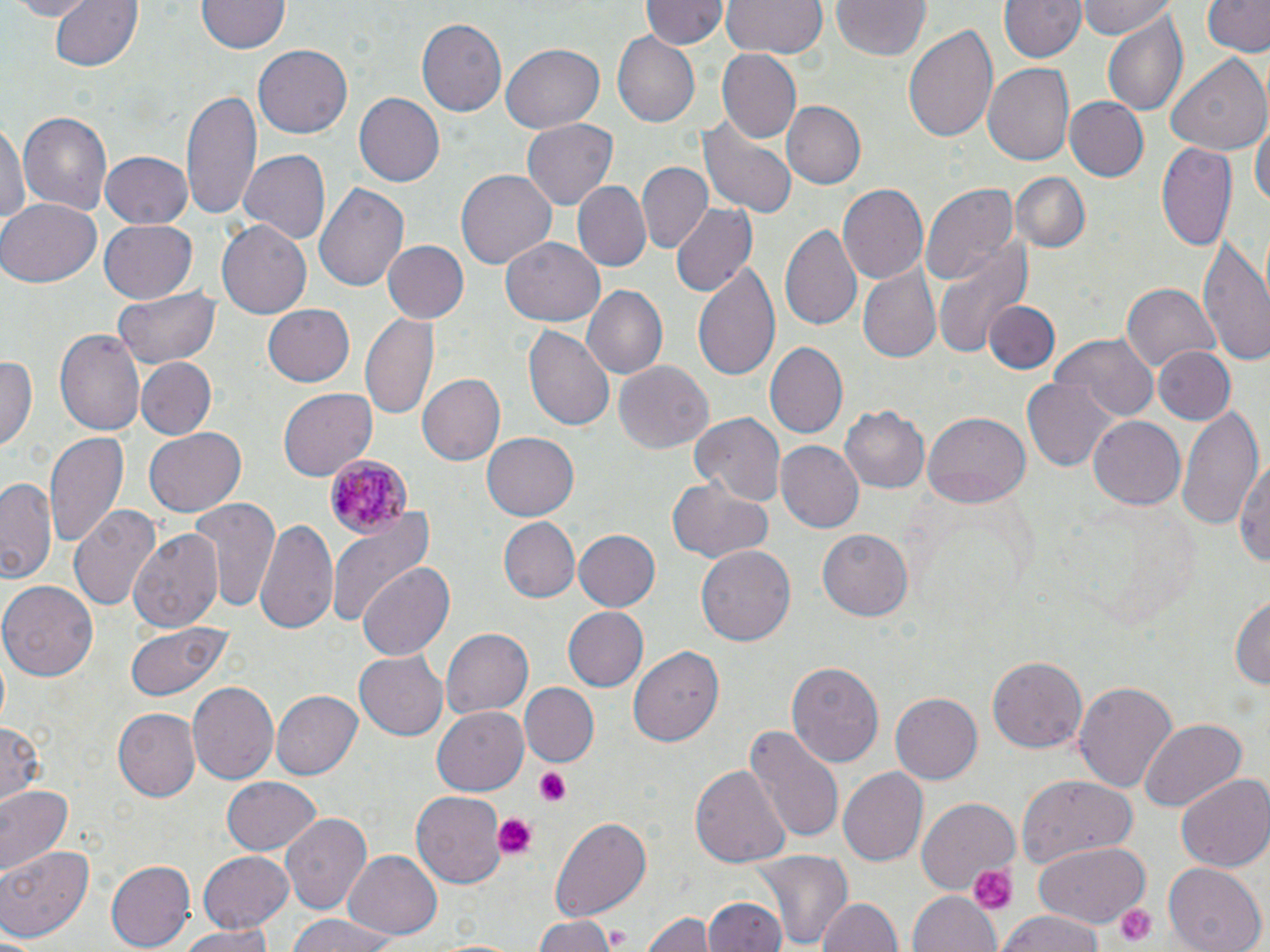

Summary:
  - Coordinate format: approximate bounding boxes as [x1, y1, x2, y2] in pixels
  - Plasmodium malariae-infected red blood cell locations: [324, 454, 413, 540]
  - Uninfected red blood cell locations: [3, 0, 100, 20], [50, 0, 145, 74], [198, 0, 288, 57], [642, 0, 725, 51], [723, 0, 826, 59], [829, 0, 932, 61], [994, 0, 1087, 65], [1078, 0, 1179, 41], [1200, 0, 1270, 60], [1098, 7, 1190, 117], [417, 18, 506, 116], [903, 24, 1000, 145], [612, 32, 700, 127], [501, 42, 605, 134], [254, 45, 354, 139], [716, 49, 801, 142], [1166, 55, 1270, 157], [982, 63, 1073, 167], [177, 85, 261, 227], [355, 93, 445, 187], [1062, 96, 1149, 182], [784, 101, 865, 188], [694, 108, 797, 220], [17, 110, 113, 216], [521, 119, 617, 210], [0, 121, 30, 231], [1252, 122, 1269, 215], [1155, 141, 1236, 251], [102, 150, 193, 229], [239, 150, 332, 244], [636, 162, 712, 253], [653, 164, 744, 276], [454, 168, 558, 273], [1014, 172, 1089, 252], [312, 179, 407, 295], [574, 183, 649, 270], [837, 183, 928, 286], [921, 183, 1020, 286], [0, 197, 99, 287], [670, 203, 758, 299], [100, 220, 198, 302], [216, 221, 311, 319], [779, 222, 861, 331], [1196, 230, 1270, 369], [501, 237, 605, 328], [933, 240, 1031, 354], [381, 241, 468, 323], [693, 258, 784, 384], [857, 266, 939, 365], [1121, 283, 1219, 374], [582, 284, 668, 380], [111, 286, 221, 369], [986, 301, 1058, 374], [264, 303, 356, 388], [361, 313, 441, 421], [523, 325, 614, 434], [55, 326, 146, 437], [1051, 334, 1161, 421], [763, 341, 847, 439], [1155, 347, 1236, 426], [0, 353, 36, 453], [137, 358, 215, 438], [612, 361, 714, 455], [419, 373, 506, 466], [1023, 378, 1119, 470], [279, 387, 376, 481], [1176, 401, 1264, 534], [839, 405, 930, 495], [923, 408, 1030, 504], [689, 411, 786, 504], [1087, 414, 1185, 508], [143, 427, 246, 518], [46, 431, 131, 551], [483, 431, 578, 521], [774, 441, 864, 533], [1234, 457, 1268, 573], [1, 476, 59, 586], [667, 479, 773, 562], [189, 496, 279, 612], [68, 503, 160, 614], [327, 505, 433, 631], [255, 515, 340, 638], [499, 517, 579, 601], [132, 528, 224, 633], [818, 528, 914, 623], [573, 529, 661, 611], [697, 543, 798, 647], [359, 562, 455, 662], [1, 580, 96, 681], [1231, 593, 1269, 694], [565, 608, 647, 690], [123, 620, 230, 701], [439, 628, 532, 720], [631, 643, 722, 746], [355, 652, 449, 740], [988, 656, 1087, 753], [786, 660, 884, 767], [1074, 679, 1178, 795], [187, 682, 279, 784], [522, 683, 597, 766], [270, 689, 362, 781], [891, 692, 983, 785], [433, 708, 528, 795], [113, 709, 200, 802], [1140, 719, 1247, 810], [0, 721, 47, 805], [744, 725, 843, 845], [691, 764, 791, 871], [838, 766, 928, 867], [1018, 774, 1134, 869], [1176, 774, 1270, 873], [221, 775, 321, 856], [0, 784, 75, 879], [411, 793, 505, 886], [916, 797, 1020, 896], [282, 811, 372, 916], [547, 816, 654, 924], [1031, 839, 1152, 926], [0, 843, 95, 943], [198, 849, 295, 931], [752, 849, 853, 952], [343, 851, 442, 939], [105, 859, 195, 951], [1162, 863, 1266, 952], [910, 891, 1001, 952], [815, 895, 904, 952], [703, 896, 788, 951], [996, 909, 1106, 952], [640, 912, 713, 952], [281, 914, 404, 952], [532, 916, 618, 952], [179, 925, 278, 952]
  - Platelet locations: [534, 768, 571, 805], [494, 813, 536, 857], [966, 860, 1017, 915], [1113, 902, 1158, 949]
  - Slide-level diagnosis: Plasmodium malariae
  - Field of view: one of a larger specimen
  - Image size: 1270×952 pixels
  - Stain: May-Grünwald-Giemsa
  - Magnification: 1000x
  - Modality: optical microscopy
  - Preparation: thin blood smear